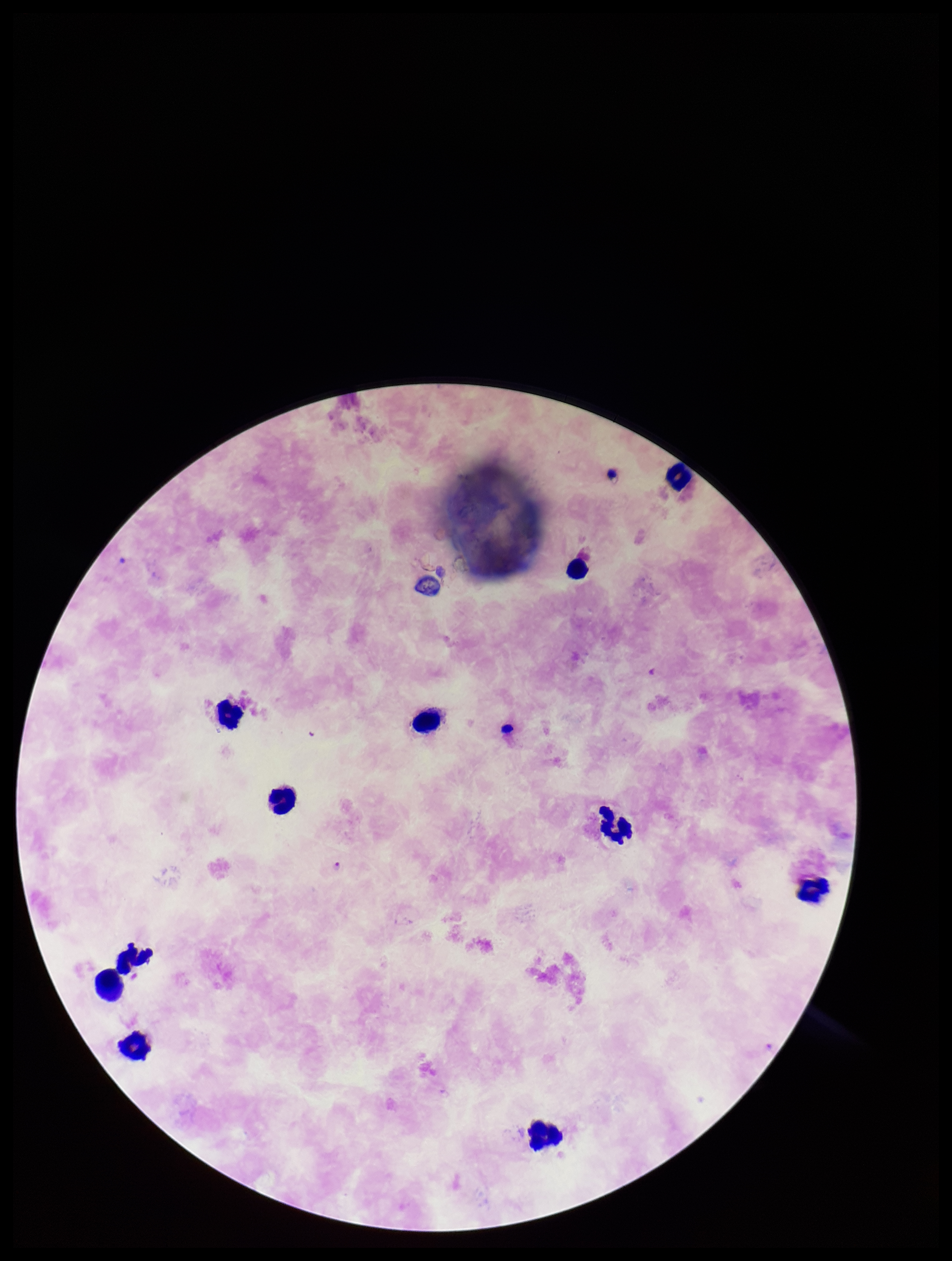
Smartphone photograph taken through the eyepiece of a microscope. Image is 952×1261 pixels. Preparation: thick. One field from this slide. Species reported for this patient: Plasmodium falciparum. Plasmodium parasites: identified. Leukocyte count: 11. Parasite count: 1. Patient malaria status: positive. Stained with Giemsa.